State the blood parasite species.
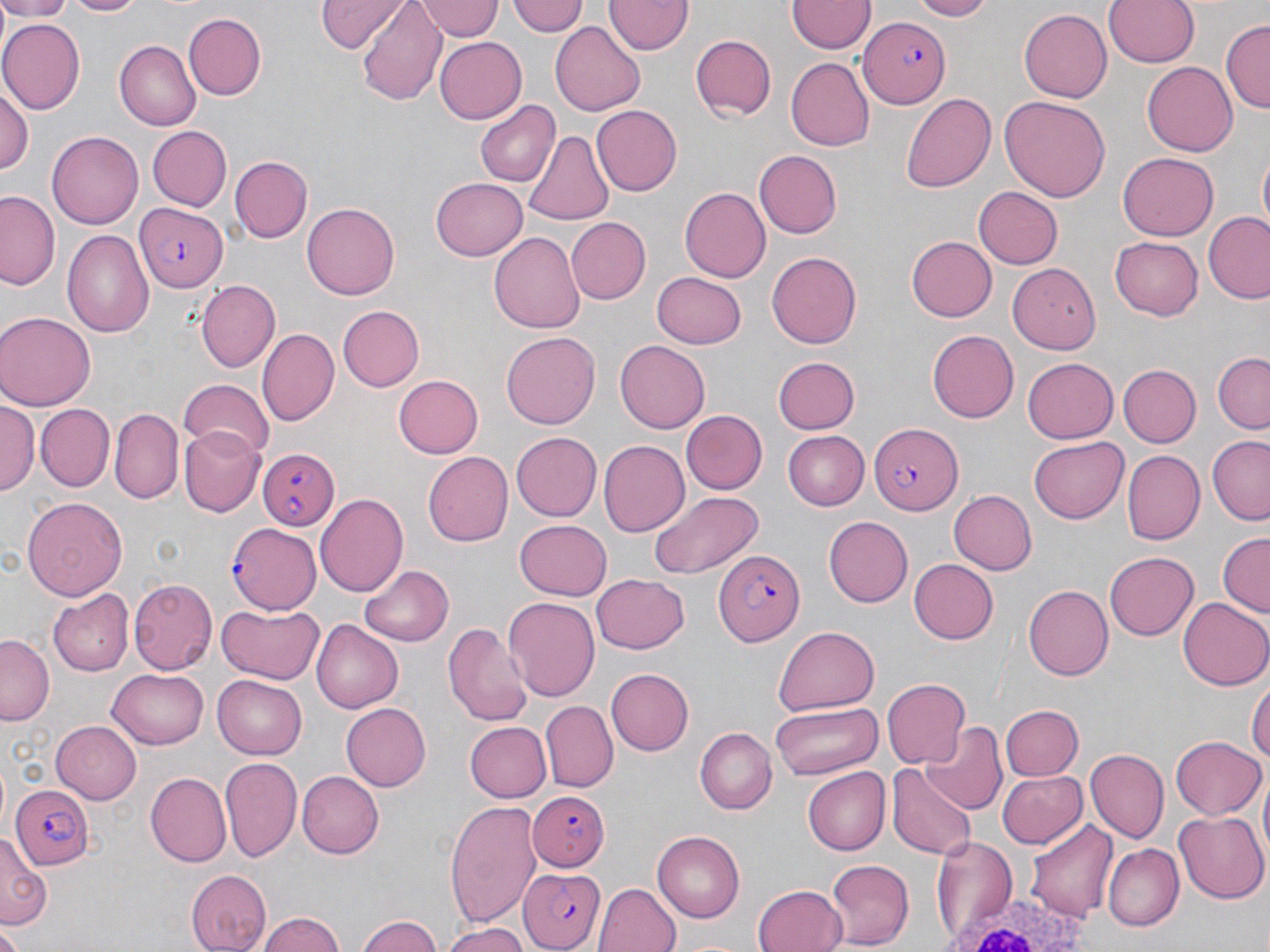

Plasmodium falciparum.

Approximate bounding boxes as [x1, y1, x2, y2] in pixels. Uninfected red blood cell locations: [0, 0, 73, 20], [66, 0, 145, 18], [316, 0, 406, 53], [508, 0, 588, 39], [605, 0, 691, 57], [905, 0, 993, 20], [1104, 0, 1200, 68], [787, 1, 872, 54], [358, 2, 447, 106], [416, 2, 504, 42], [1020, 7, 1116, 103], [184, 12, 267, 100], [0, 19, 84, 111], [1221, 19, 1270, 114], [550, 22, 646, 115], [691, 34, 776, 120], [435, 35, 527, 122], [117, 39, 205, 131], [786, 57, 875, 151], [1141, 61, 1237, 155], [0, 86, 33, 177], [899, 93, 997, 192], [999, 94, 1109, 203], [474, 98, 559, 187], [593, 104, 686, 196], [147, 126, 232, 211], [524, 127, 617, 223], [48, 129, 148, 229], [1257, 150, 1270, 235], [754, 151, 843, 237], [1118, 154, 1218, 240], [232, 156, 311, 241], [430, 177, 527, 262], [973, 185, 1063, 269], [678, 187, 770, 284], [1, 192, 62, 292], [300, 202, 400, 300], [1202, 210, 1270, 305], [566, 216, 651, 304], [61, 229, 155, 340], [488, 232, 583, 336], [904, 234, 995, 323], [1110, 235, 1204, 319], [766, 250, 863, 349], [1007, 263, 1099, 353], [652, 271, 746, 347], [198, 279, 280, 372], [334, 303, 424, 389], [0, 311, 95, 409], [256, 329, 338, 427], [927, 329, 1018, 422], [502, 332, 599, 429], [615, 340, 709, 432], [1213, 353, 1270, 433], [773, 354, 860, 432], [1024, 355, 1119, 441], [1119, 365, 1200, 447], [393, 374, 484, 458], [178, 378, 275, 456], [0, 401, 39, 497], [37, 405, 113, 489], [110, 408, 183, 503], [680, 410, 767, 495], [178, 427, 262, 514], [783, 431, 872, 510], [511, 432, 602, 522], [1029, 436, 1129, 525], [1207, 439, 1269, 524], [597, 440, 689, 537], [423, 450, 512, 547], [1122, 451, 1204, 546], [947, 489, 1036, 575], [649, 490, 765, 581], [315, 494, 408, 596], [23, 496, 125, 604], [824, 516, 913, 607], [516, 517, 612, 598], [1218, 533, 1269, 617], [1104, 551, 1197, 641], [907, 559, 1000, 643], [360, 564, 454, 646], [590, 574, 689, 654], [128, 578, 215, 673], [1025, 585, 1113, 681], [47, 589, 132, 677], [501, 596, 599, 703], [1180, 596, 1270, 690], [217, 603, 325, 684], [311, 618, 402, 712], [445, 620, 532, 726], [773, 625, 881, 715], [1, 634, 52, 725], [106, 669, 209, 750], [605, 669, 692, 755], [214, 674, 308, 757], [1248, 675, 1269, 777], [881, 679, 971, 769], [772, 700, 883, 780], [540, 701, 617, 791], [341, 702, 431, 790], [999, 704, 1082, 783], [465, 720, 550, 803], [52, 721, 144, 803], [920, 722, 1007, 815], [696, 728, 775, 813], [1170, 736, 1264, 819], [1086, 748, 1170, 843], [220, 756, 302, 860], [889, 764, 974, 859], [802, 765, 890, 855], [995, 769, 1087, 849], [145, 772, 230, 866], [296, 772, 384, 858], [445, 801, 542, 925], [1172, 810, 1268, 903], [1026, 819, 1116, 923], [653, 830, 748, 922], [1, 836, 48, 927], [930, 836, 1018, 940], [1104, 842, 1184, 930], [825, 858, 914, 947], [184, 868, 273, 951], [596, 882, 680, 952], [754, 884, 846, 952], [258, 911, 348, 952], [355, 914, 447, 952], [438, 924, 532, 952], [0, 928, 22, 952]. Plasmodium falciparum-infected red blood cell locations: [861, 18, 952, 109], [137, 205, 227, 291], [868, 424, 960, 514], [256, 448, 337, 532], [228, 521, 321, 612], [716, 548, 807, 646], [13, 783, 94, 869], [525, 788, 607, 870], [518, 865, 606, 950]. White blood cell locations: [946, 890, 1094, 952]. Thin blood film. May-Grünwald-Giemsa stain. Light microscopy. Single field of view. Image is 1270×952 pixels. Captured at 1000x magnification.